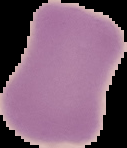
Summary:
  - Malaria status: uninfected
  - Image size: 127×148 pixels
  - Image type: segmented cell region on a black background
  - Preparation: thin blood film